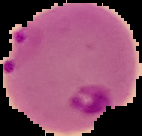
preparation = thin blood smear
image type = cell region segmented out of the field of view; surrounding area masked to black
image size = 142×136 pixels
malaria status = parasitized